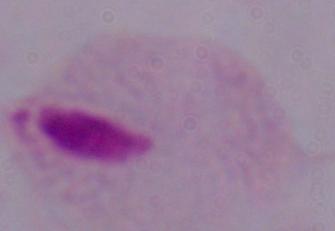
Summary:
  - Modality: photomicrograph
  - Magnification: 1000x
  - Identification: trichomonad